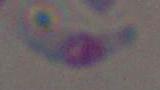
1000x magnification. Photomicrograph. Toxoplasma gondii is seen.